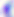
Summary:
  - Modality: micrograph
  - Magnification: 400x
  - Identification: Toxoplasma gondii